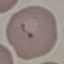
Malaria status: parasitized. Cell patch, automatically extracted from a larger field of view and resized to 64 × 64 pixels. Giemsa stain. Photographed with a smartphone camera at the microscope eyepiece. Thin blood smear.